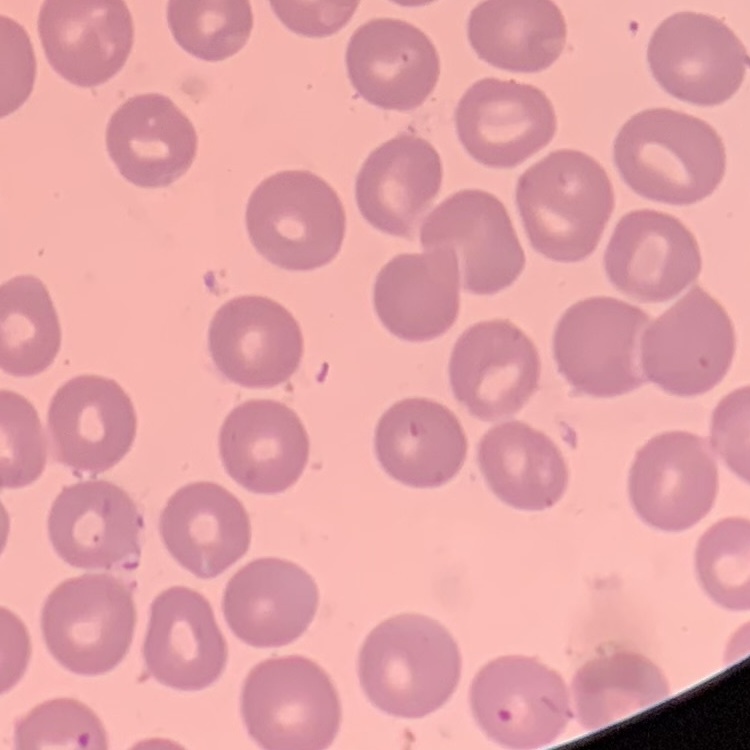
The erythrocytes exhibit no rouleaux formation. Thin blood film. Square crop of a larger photomicrograph. Stained with either Field's or Giemsa.